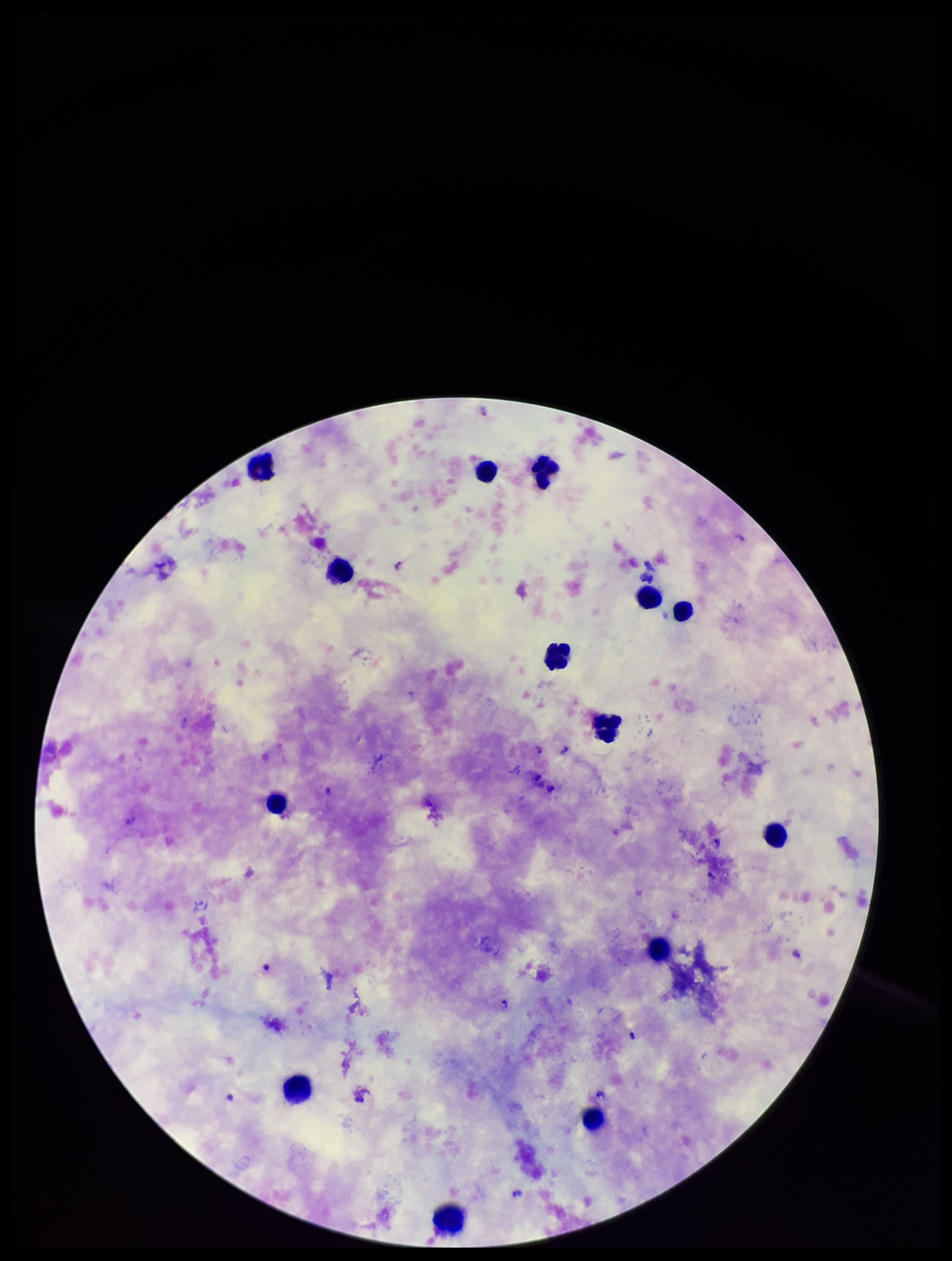 Patient malaria status: positive. Giemsa stain. Smartphone photograph taken through the eyepiece of a microscope. Preparation: thick blood smear. Plasmodium parasites: identified. Leukocyte count: 14. Image is 952×1261 pixels. Species reported for this patient: Plasmodium falciparum. Parasite count: 17. Single field of view.